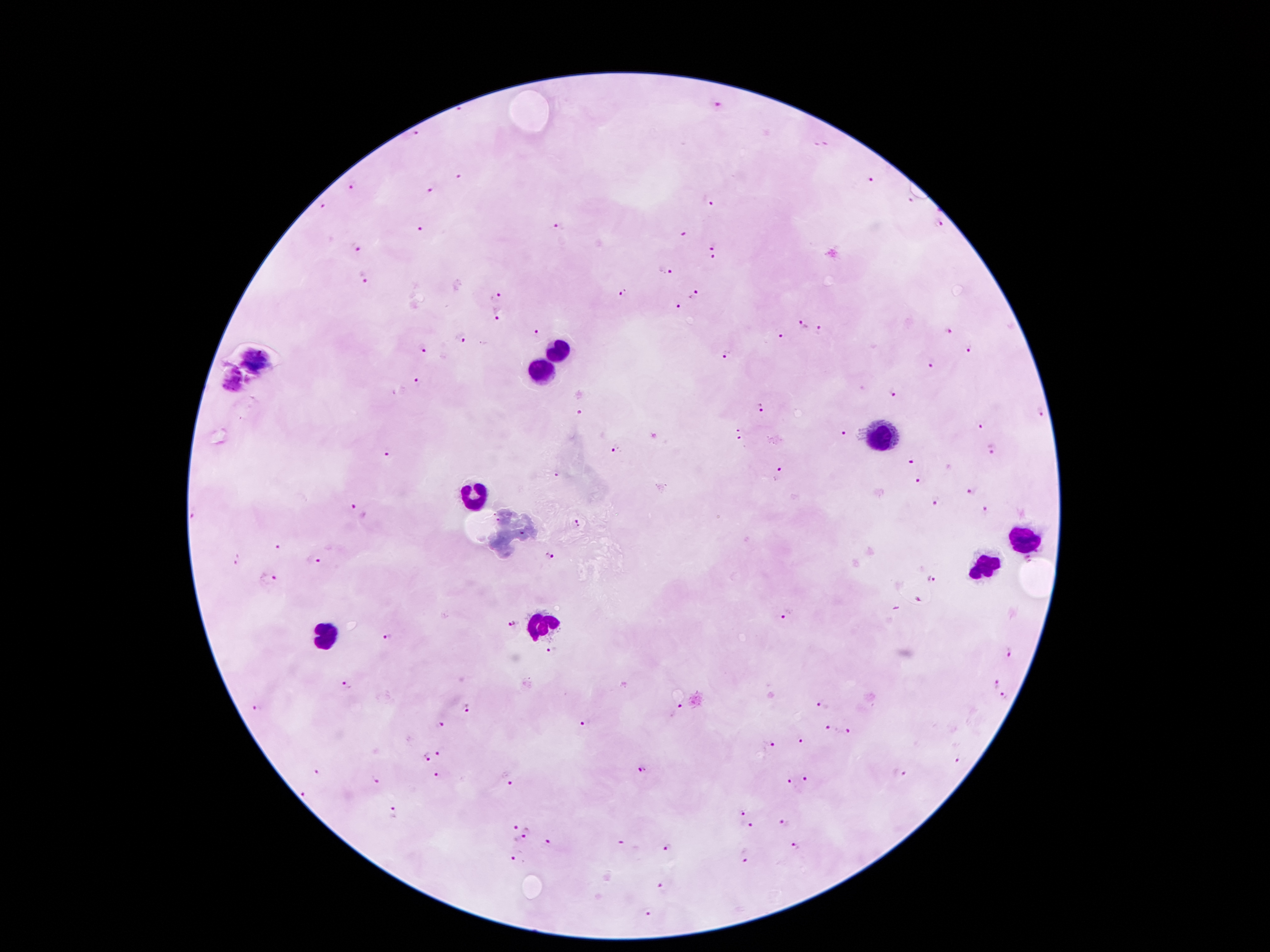 Approximate centers as {x, y} in pixels. Leukocyte locations: {559, 351}, {541, 372}, {877, 435}, {472, 493}, {1026, 537}, {982, 564}, {541, 626}, {325, 637}. Malaria parasite locations: {718, 103}, {460, 112}, {413, 132}, {815, 142}, {829, 142}, {459, 177}, {869, 180}, {352, 186}, {432, 191}, {709, 200}, {910, 200}, {320, 205}, {560, 222}, {938, 225}, {420, 229}, {684, 236}, {713, 245}, {355, 248}, {713, 259}, {666, 272}, {362, 279}, {622, 292}, {694, 295}, {497, 296}, {679, 307}, {498, 314}, {803, 322}, {822, 329}, {946, 332}, {537, 335}, {779, 336}, {461, 338}, {422, 347}, {971, 348}, {727, 354}, {932, 362}, {417, 383}, {891, 394}, {764, 408}, {1040, 412}, {582, 414}, {982, 424}, {738, 429}, {844, 431}, {740, 440}, {614, 449}, {993, 449}, {387, 454}, {911, 462}, {780, 473}, {554, 475}, {921, 479}, {970, 491}, {937, 499}, {350, 508}, {984, 511}, {577, 525}, {278, 548}, {550, 557}, {318, 559}, {235, 560}, {269, 578}, {930, 581}, {789, 615}, {511, 624}, {386, 638}, {1005, 650}, {553, 653}, {995, 683}, {348, 686}, {1003, 697}, {822, 706}, {255, 708}, {469, 709}, {677, 712}, {587, 723}, {440, 725}, {832, 729}, {846, 733}, {802, 742}, {766, 745}, {440, 753}, {424, 757}, {959, 762}, {645, 770}, {318, 773}, {436, 775}, {900, 775}, {507, 779}, {376, 780}, {808, 781}, {789, 782}, {305, 796}, {739, 808}, {396, 811}, {523, 823}, {783, 824}, {745, 825}, {520, 840}, {548, 842}, {620, 845}, {795, 845}, {667, 847}, {744, 856}, {518, 857}, {663, 886}, {647, 913}. Single field of view. Patient malaria status: positive for Plasmodium falciparum. Thick blood film. Photographed through the microscope eyepiece with a smartphone camera. Image is 1270×952 pixels. 100x magnification. Giemsa-stained preparation.